Locate and identify every blood parasite.
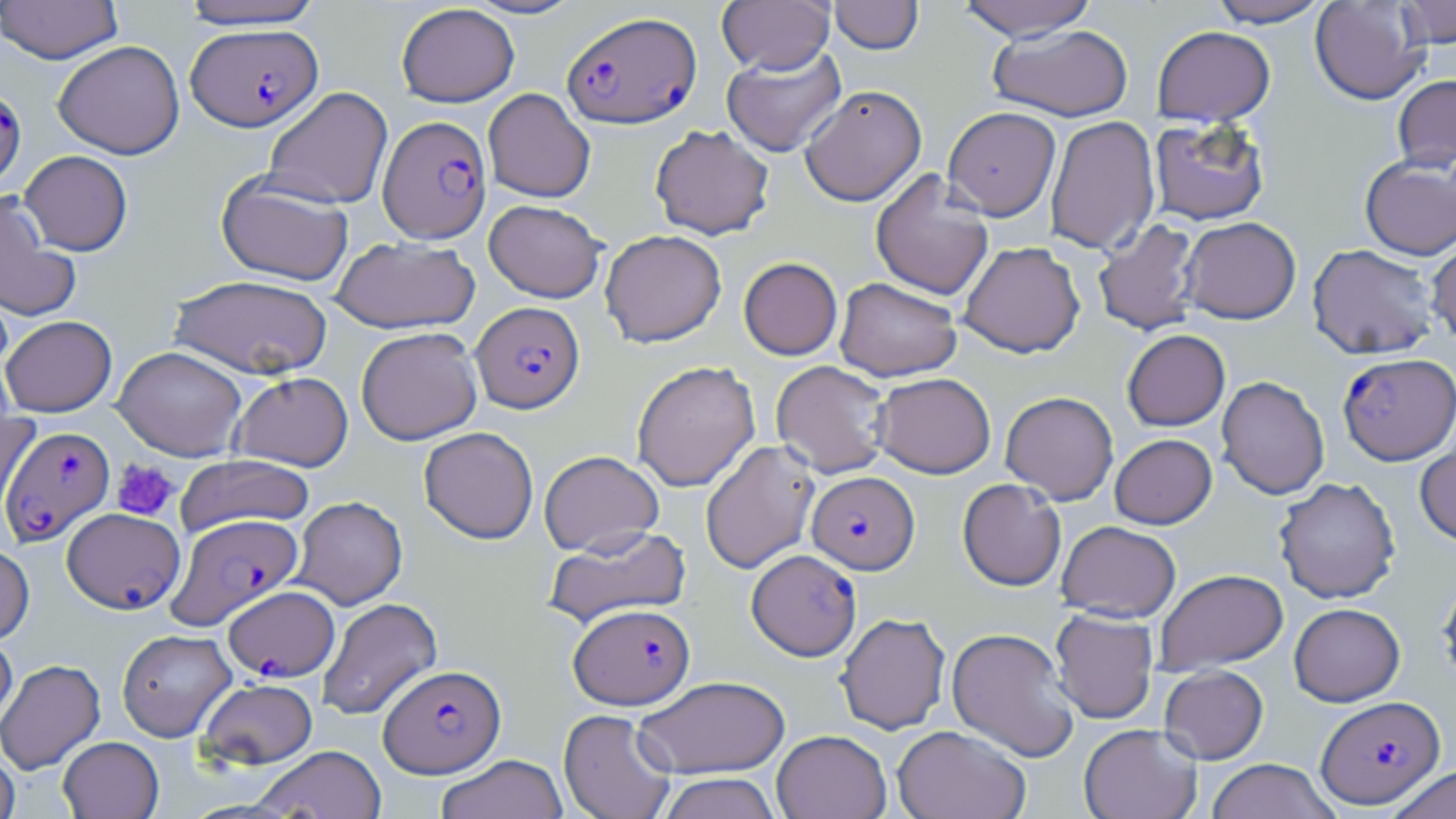

Approximate bounding boxes as (x1,y1)-(x2,y2) corner pairs in pixels.
Plasmodium falciparum-infected red blood cells (subset): (562,10)-(701,129), (186,24)-(322,131), (0,85)-(26,188), (378,115)-(491,242), (471,301)-(584,413), (1337,352)-(1456,465), (2,426)-(114,545), (807,471)-(919,574), (167,513)-(303,629), (746,549)-(862,660), (224,586)-(339,681), (569,603)-(695,709), (379,663)-(506,777), (1315,695)-(1445,808).
No Plasmodium ovale, Plasmodium malariae, Plasmodium vivax, Babesia divergens, or Trypanosoma brucei observed.

Summary:
  - Platelet locations: (111,459)-(179,521)
  - Uninfected red blood cell locations (subset): (178,0)-(328,30), (463,0)-(585,20), (717,0)-(835,74), (829,0)-(923,54), (955,0)-(1100,40), (1207,0)-(1331,28), (1309,0)-(1430,105), (1397,0)-(1456,48), (0,1)-(123,63), (396,4)-(520,107), (988,24)-(1134,121), (1151,25)-(1275,126), (53,40)-(185,159), (722,46)-(847,157), (1392,74)-(1456,172), (800,84)-(927,206), (262,86)-(392,210), (483,88)-(595,202), (943,107)-(1061,220), (1045,115)-(1160,254), (1148,117)-(1270,226), (649,124)-(775,240), (19,150)-(133,256), (1359,157)-(1456,261), (870,168)-(994,300), (216,172)-(355,286), (0,190)-(81,322), (484,199)-(606,302), (1180,217)-(1301,324), (1092,219)-(1201,336), (600,229)-(726,347), (1426,232)-(1456,345), (330,236)-(480,334), (959,241)-(1085,358), (1307,243)-(1440,360), (739,257)-(843,360), (169,275)-(334,379), (834,277)-(962,381), (1,315)-(117,417), (356,327)-(483,445), (1122,329)-(1230,431), (113,346)-(246,460), (631,360)-(760,492), (771,360)-(892,478), (229,371)-(354,471), (873,372)-(996,478), (1216,376)-(1329,499), (1000,391)-(1118,504), (0,412)-(40,522), (419,426)-(538,544), (1415,431)-(1456,547), (1110,433)-(1217,529), (700,440)-(820,574), (539,450)-(664,555), (175,455)-(315,536), (1274,477)-(1400,603), (957,478)-(1067,591), (292,496)-(407,609), (1057,520)-(1181,621), (542,525)-(691,628), (0,542)-(35,645), (1154,569)-(1288,674), (1437,572)-(1456,691), (316,597)-(442,721), (1289,603)-(1405,706), (1049,609)-(1159,724), (836,612)-(951,734), (946,627)-(1080,762), (117,629)-(236,741), (0,630)-(17,732), (0,658)-(106,775), (1159,665)-(1268,764), (634,675)-(790,778), (197,678)-(318,769), (558,709)-(677,819), (1078,723)-(1202,819), (892,725)-(1031,819), (772,730)-(891,819), (58,736)-(164,818), (252,745)-(387,818), (0,746)-(20,819), (435,754)-(569,819), (1206,758)-(1339,819), (1385,765)-(1455,819), (656,772)-(782,819)
  - Slide-level diagnosis: Plasmodium falciparum
  - Magnification: 1000x
  - Modality: light microscopy
  - Stain: May-Grünwald-Giemsa
  - Field of view: single
  - Preparation: thin blood film
  - Image size: 1456×819 pixels